Locate every blood parasite and identify its species.
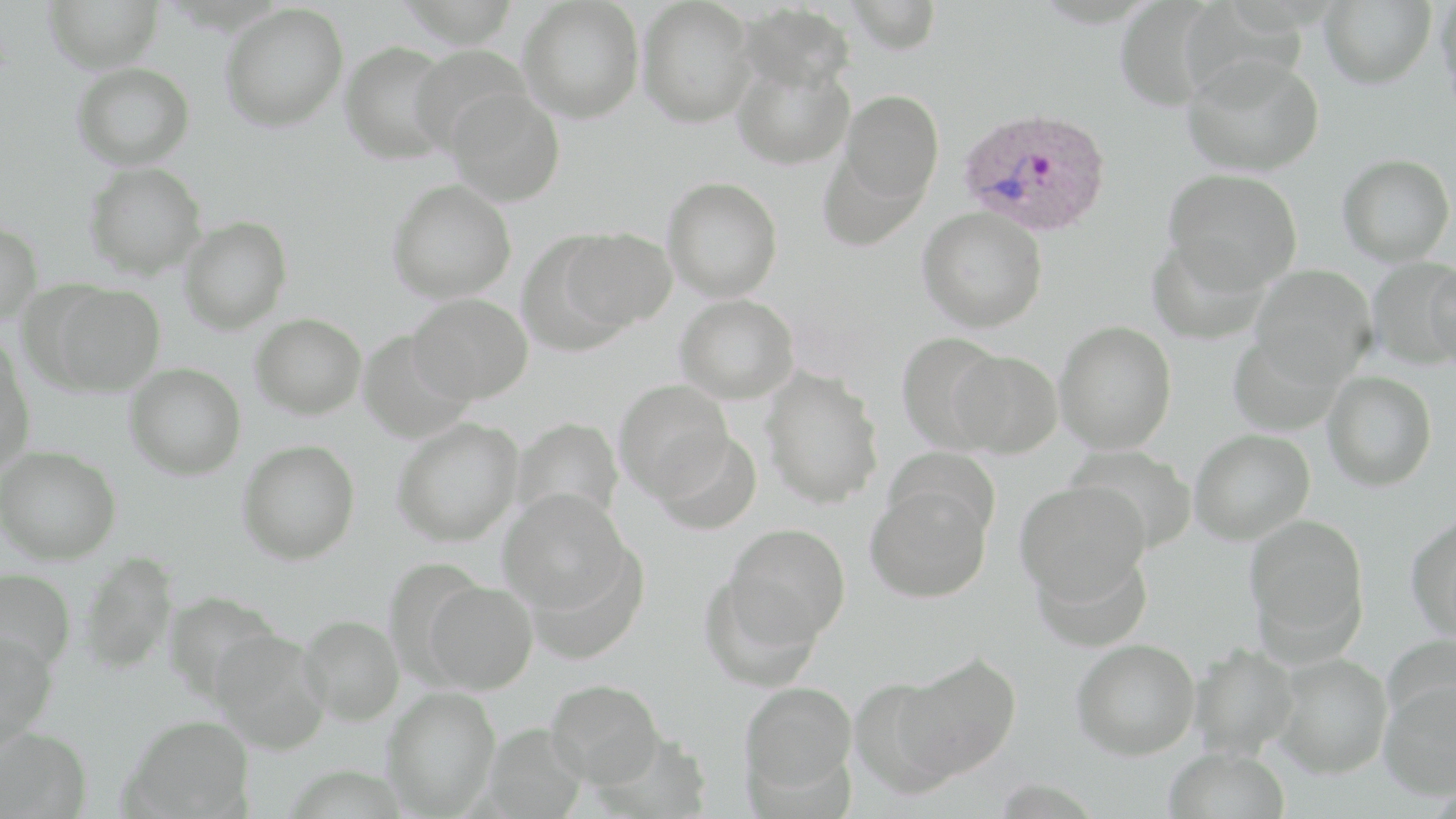

Approximate bounding boxes as (x1, y1, x2, y2) in pixels.
Plasmodium ovale-infected red blood cells: (956, 105, 1112, 237).
No Plasmodium falciparum, Plasmodium malariae, Plasmodium vivax, Babesia divergens, or Trypanosoma brucei observed.

slide_level_diagnosis: Plasmodium ovale
image_size: 1456×819 pixels
stain: May-Grünwald-Giemsa
magnification: 1000x
modality: optical microscopy
uninfected_red_blood_cell_locations: 'approximate bounding boxes as (x1, y1, x2, y2) in pixels: (44, 0, 164, 73), (518, 0, 645, 123), (637, 0, 757, 127), (846, 0, 943, 54), (1319, 0, 1436, 89), (1436, 0, 1456, 114), (220, 2, 349, 132), (737, 3, 855, 94), (340, 40, 455, 164), (408, 44, 531, 154), (1183, 54, 1324, 177), (732, 58, 854, 170), (72, 62, 195, 169), (447, 89, 566, 206), (839, 90, 944, 204), (1338, 153, 1454, 266), (84, 161, 207, 279), (1163, 168, 1302, 293), (662, 176, 783, 302), (387, 179, 516, 303), (917, 207, 1048, 332), (179, 216, 292, 335), (0, 220, 43, 324), (560, 227, 677, 331), (1148, 236, 1270, 346), (1366, 258, 1456, 370), (1424, 258, 1456, 370), (1251, 264, 1377, 385), (39, 282, 166, 396), (407, 292, 533, 404), (675, 293, 800, 403), (250, 312, 367, 419), (1054, 321, 1177, 454), (357, 330, 475, 444), (896, 332, 1006, 452), (1228, 334, 1345, 436), (0, 339, 35, 474), (949, 349, 1062, 458), (124, 363, 246, 480), (760, 366, 883, 509), (1322, 371, 1438, 491), (614, 378, 736, 500), (512, 416, 624, 529), (391, 417, 524, 546), (650, 428, 762, 535), (1189, 429, 1315, 544), (238, 439, 360, 564), (1, 445, 121, 564), (1069, 445, 1197, 554), (886, 446, 999, 545), (1015, 480, 1150, 606), (865, 484, 992, 602), (497, 487, 633, 615), (1406, 513, 1456, 640), (1244, 514, 1368, 648), (724, 523, 851, 646), (1033, 546, 1152, 653), (78, 550, 178, 676), (0, 567, 77, 673), (423, 580, 538, 694), (164, 591, 285, 703), (300, 614, 405, 725), (209, 629, 331, 755), (0, 630, 57, 749), (1072, 638, 1200, 760), (1190, 643, 1300, 759), (1272, 652, 1393, 778), (895, 654, 1021, 780), (849, 676, 964, 798), (546, 677, 665, 787), (739, 680, 857, 799), (1378, 680, 1456, 800), (382, 685, 501, 816), (124, 714, 254, 817), (0, 726, 93, 818), (1163, 746, 1290, 819)'
preparation: thin blood film
field_of_view: one of a larger specimen